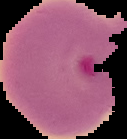 From a thin blood film. Image is 127×139 pixels. Cell region segmented out of the field of view; the surrounding area is masked to black. Result: Plasmodium parasites detected.